State which parasite is depicted.
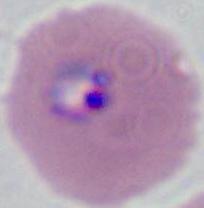

This is Plasmodium.

{
  "modality": "micrograph",
  "magnification": "400x or 1000x"
}